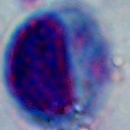

magnification = 1000x
modality = micrograph
identification = leukocyte